Name the parasite shown.
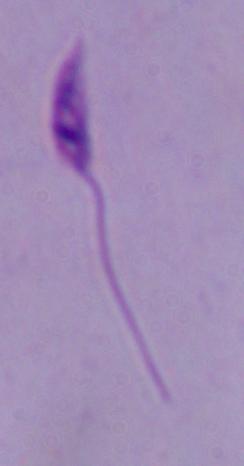
This is Leishmania.

Photomicrograph. Captured at 1000x magnification.